Comment on the morphology of the red blood cells.
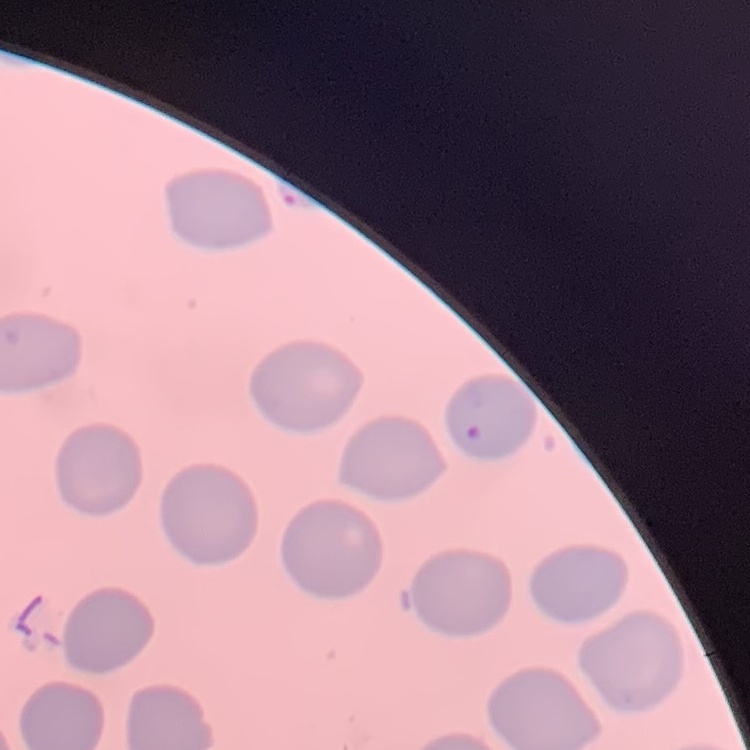

They show no rouleaux formation.

preparation = thin blood smear
image type = square crop of a larger photomicrograph
stain = Field's or Giemsa